Report the malaria status of this cell.
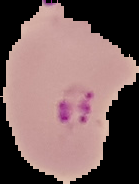

Parasitized.

Segmented cell region on a black background. From a thin blood film. Image is 139×184 pixels.